Classify this cell by malaria status.
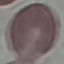

It is uninfected.

capture = smartphone through the microscope eyepiece
preparation = thin blood smear
image type = cell patch, automatically extracted from a larger field of view and resized to 64 × 64 pixels
stain = Giemsa